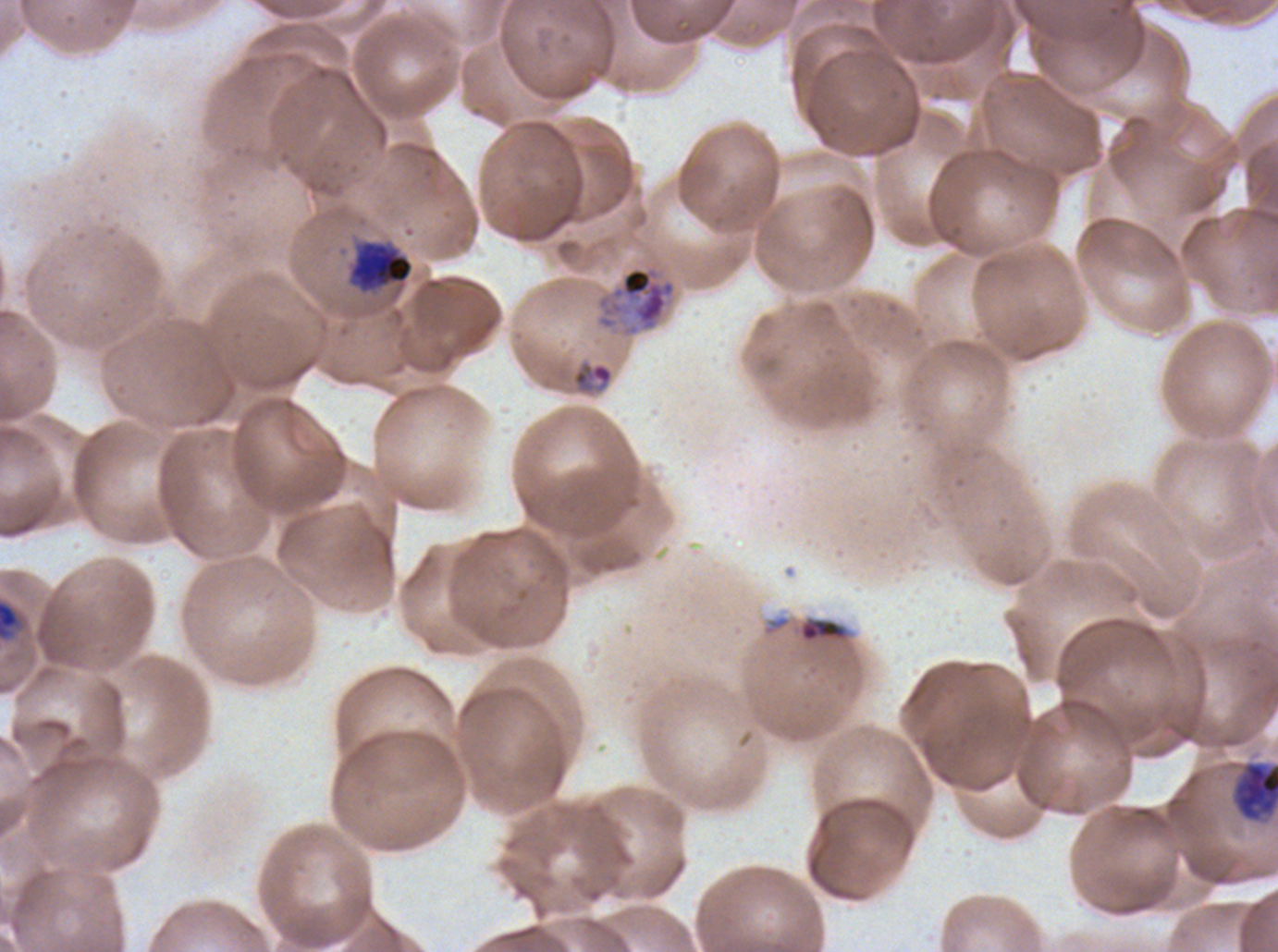

Approximate bounding rectangles given as corner coordinates in pixels from the top-left. Debris locations: (x1=0, y1=599, x2=20, y2=640), (x1=799, y1=618, x2=846, y2=641). Late trophozoite locations: (x1=594, y1=262, x2=678, y2=339). Ring locations: (x1=571, y1=360, x2=614, y2=394). Early schizont locations: (x1=347, y1=238, x2=414, y2=295), (x1=1233, y1=761, x2=1277, y2=823). Image is 1278×952 pixels. A sub-image separated from a larger composite. Life-cycle stages observed: ring, late trophozoite, early schizont. Thin blood smear. Giemsa stain. P. falciparum cultured ex vivo for 24 to 48 hours, from a patient in The Gambia.